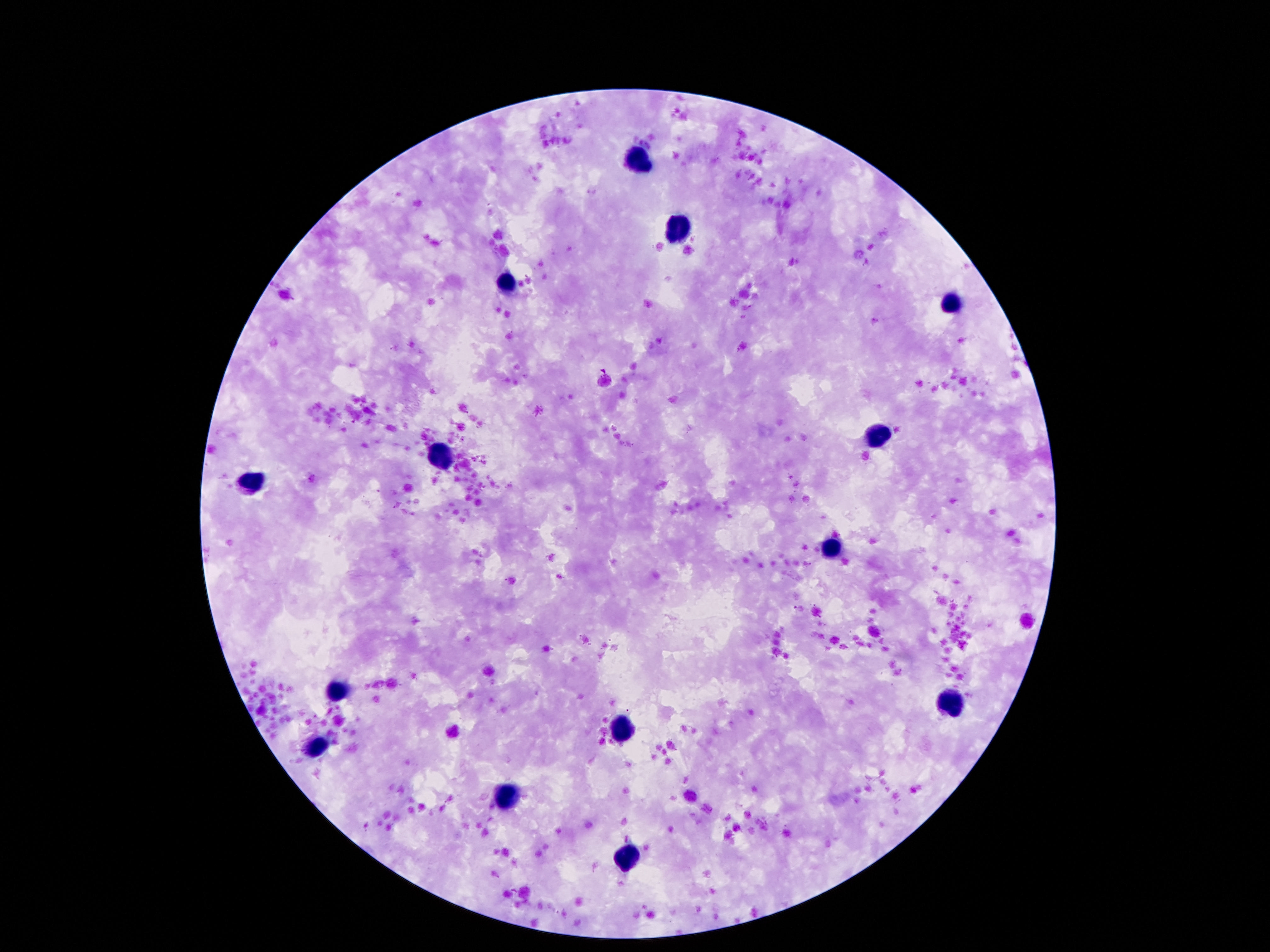
stain = Giemsa
field of view = one from this slide
magnification = 100x
capture = smartphone camera through the microscope eyepiece
preparation = thick peripheral-blood smear
leukocyte locations = approximate centers as (x, y) in pixels: (640, 161), (677, 227), (507, 285), (953, 302), (877, 436), (440, 451), (253, 479), (830, 548), (339, 691), (951, 700), (623, 728), (317, 748), (507, 797), (627, 863)
patient malaria status = not infected
image size = 1270×952 pixels